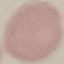
{
  "result": "no malaria parasites seen",
  "stain": "Giemsa",
  "image_type": "cell patch, automatically extracted from a larger field of view and resized to 64 × 64 pixels",
  "capture": "smartphone camera at the microscope eyepiece",
  "preparation": "thin blood smear"
}